Evaluate for malaria.
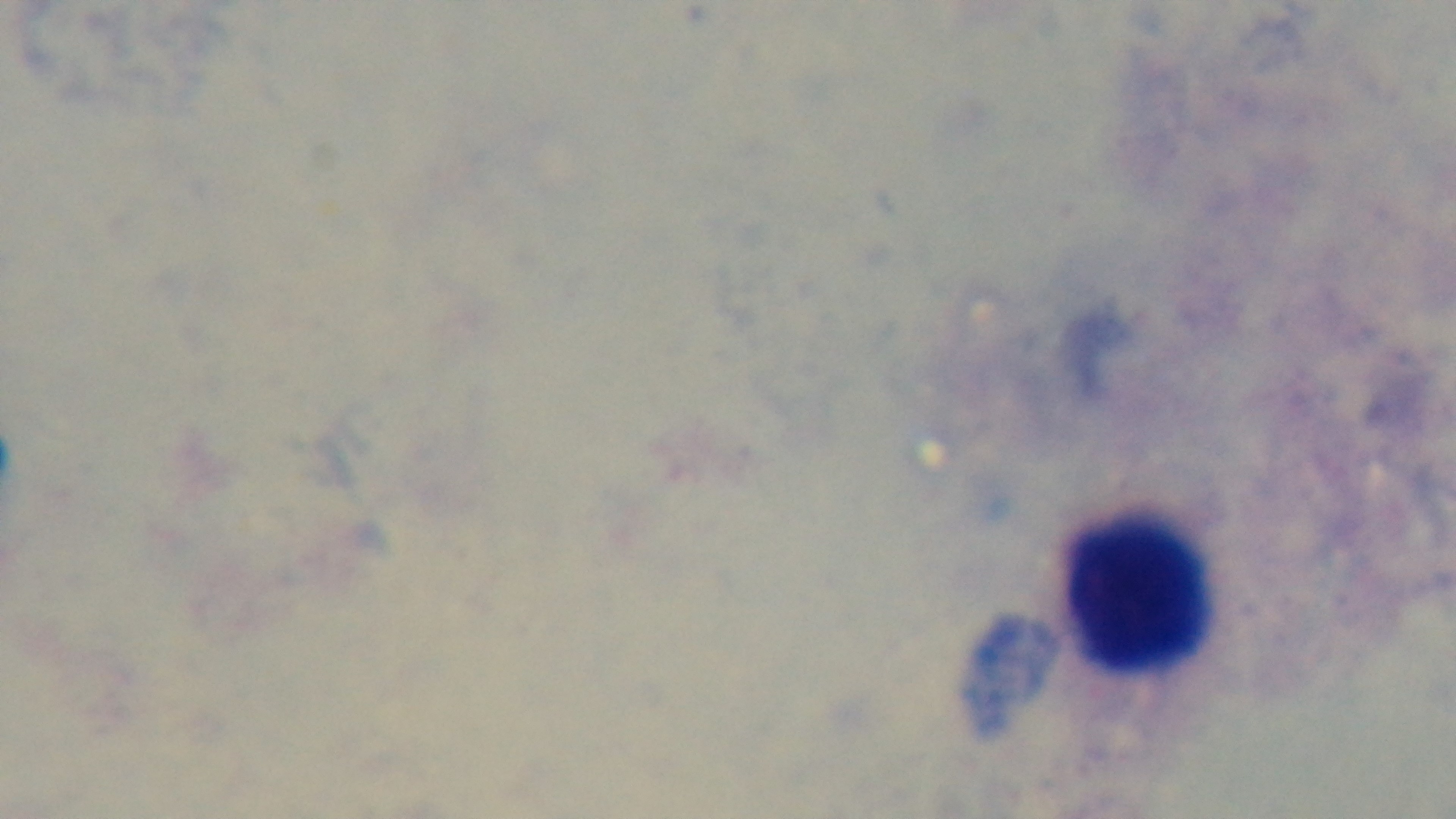

Uninfected.

Summary:
  - Objective: 100x oil immersion
  - Modality: light microscopy
  - Field of view: one from the slide
  - Capture: mounted 4K digital camera
  - Preparation: thick
  - Stain: Giemsa